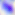 Photomicrograph. Toxoplasma gondii is shown. Captured at 400x magnification.